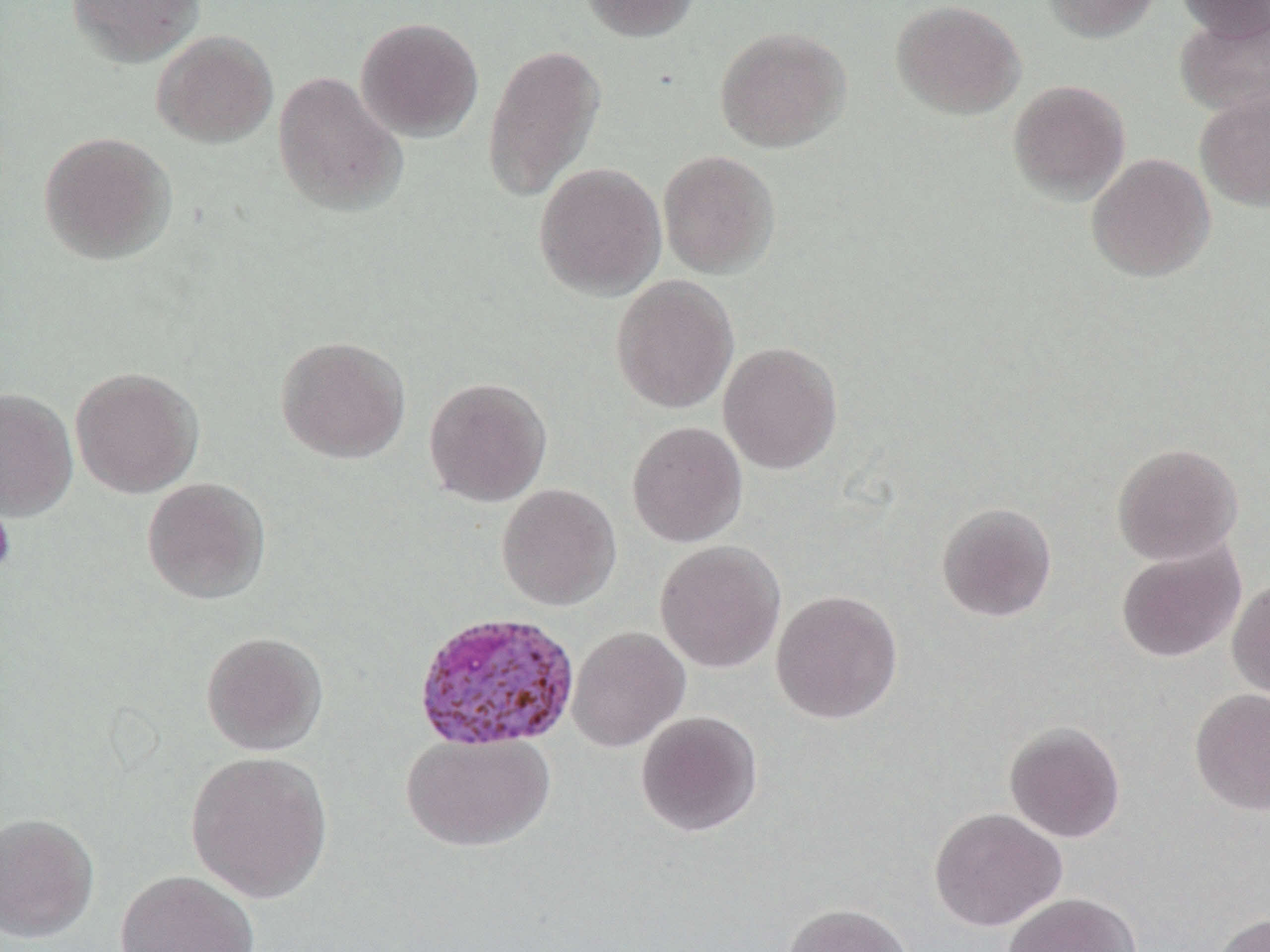

slide_level_diagnosis: Plasmodium ovale
image_size: 1270×952 pixels
preparation: thin blood film
uninfected_red_blood_cell_locations: 'approximate bounding boxes as named x1/y1/x2/y2 corners in pixels: (x1=66, y1=0, x2=205, y2=66), (x1=579, y1=0, x2=701, y2=42), (x1=1041, y1=0, x2=1162, y2=43), (x1=1175, y1=0, x2=1270, y2=43), (x1=890, y1=1, x2=1026, y2=119), (x1=1174, y1=12, x2=1270, y2=117), (x1=355, y1=17, x2=484, y2=143), (x1=714, y1=26, x2=851, y2=153), (x1=152, y1=30, x2=278, y2=148), (x1=481, y1=43, x2=606, y2=202), (x1=273, y1=71, x2=408, y2=216), (x1=1008, y1=80, x2=1130, y2=204), (x1=1194, y1=90, x2=1270, y2=212), (x1=38, y1=130, x2=177, y2=265), (x1=657, y1=151, x2=780, y2=278), (x1=1086, y1=153, x2=1216, y2=282), (x1=534, y1=162, x2=666, y2=300), (x1=610, y1=275, x2=739, y2=414), (x1=275, y1=335, x2=411, y2=464), (x1=718, y1=341, x2=843, y2=475), (x1=71, y1=367, x2=204, y2=498), (x1=424, y1=376, x2=552, y2=507), (x1=0, y1=387, x2=78, y2=521), (x1=626, y1=421, x2=748, y2=547), (x1=1112, y1=442, x2=1243, y2=565), (x1=142, y1=477, x2=271, y2=605), (x1=496, y1=484, x2=621, y2=611), (x1=936, y1=502, x2=1057, y2=622), (x1=654, y1=541, x2=786, y2=673), (x1=1116, y1=543, x2=1245, y2=663), (x1=1227, y1=577, x2=1270, y2=703), (x1=770, y1=589, x2=903, y2=724), (x1=566, y1=626, x2=690, y2=752), (x1=201, y1=631, x2=329, y2=756), (x1=1189, y1=687, x2=1270, y2=815), (x1=635, y1=710, x2=763, y2=837), (x1=1003, y1=721, x2=1126, y2=843), (x1=401, y1=733, x2=555, y2=851), (x1=186, y1=751, x2=334, y2=904), (x1=929, y1=807, x2=1067, y2=931), (x1=0, y1=812, x2=99, y2=942), (x1=116, y1=869, x2=259, y2=952), (x1=1001, y1=892, x2=1142, y2=952), (x1=781, y1=903, x2=915, y2=952), (x1=1211, y1=912, x2=1270, y2=952)'
modality: light microscopy
magnification: 1000x
field_of_view: single
platelet_locations: 'approximate bounding boxes as named x1/y1/x2/y2 corners in pixels: (x1=0, y1=499, x2=16, y2=578)'
plasmodium_ovale_infected_red_blood_cell_locations: 'approximate bounding boxes as named x1/y1/x2/y2 corners in pixels: (x1=413, y1=610, x2=580, y2=751)'